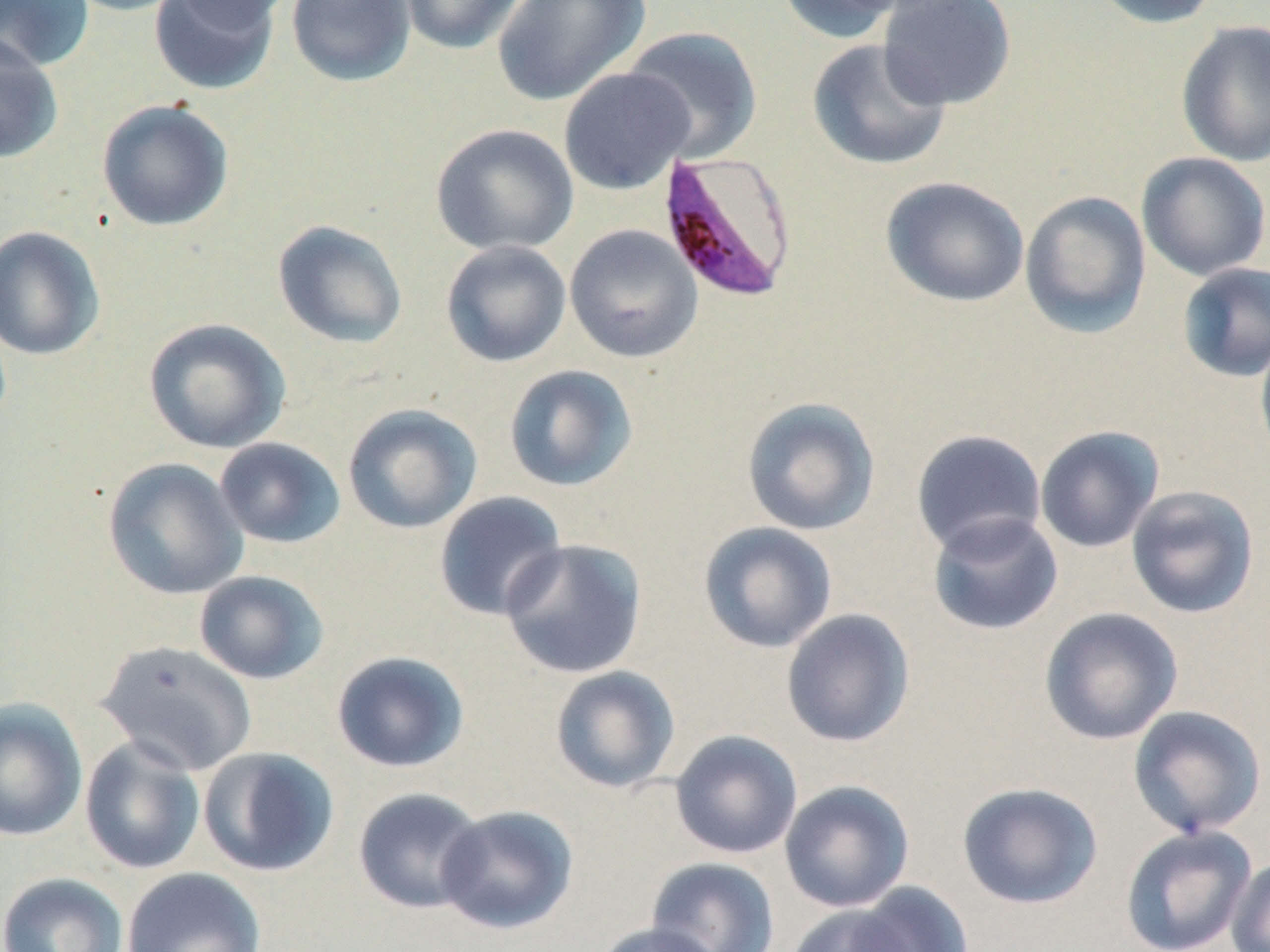 Approximate bounding boxes as (x1,y1)-(x2,y2) corner pairs in pixels. Uninfected red blood cell locations: (0,0)-(94,72), (57,0)-(190,17), (148,0)-(281,96), (164,0)-(293,31), (286,0)-(416,88), (398,0)-(528,55), (492,0)-(651,107), (774,0)-(914,44), (878,0)-(1017,110), (1085,0)-(1223,29), (1175,20)-(1270,168), (622,27)-(764,163), (0,31)-(63,164), (806,38)-(952,171), (558,67)-(695,195), (96,99)-(234,231), (430,123)-(579,256), (1136,152)-(1270,282), (881,176)-(1030,308), (1020,191)-(1151,338), (272,219)-(408,350), (564,223)-(703,363), (0,225)-(106,361), (440,240)-(572,367), (1177,262)-(1270,383), (143,317)-(291,454), (1255,333)-(1270,464), (503,364)-(638,492), (741,397)-(881,536), (342,403)-(483,534), (1034,425)-(1165,554), (910,429)-(1047,557), (214,437)-(346,549), (101,457)-(249,600), (1126,485)-(1260,619), (433,491)-(568,622), (927,512)-(1064,636), (698,521)-(838,654), (499,538)-(648,679), (193,570)-(328,684), (1038,606)-(1184,745), (780,608)-(916,747), (95,640)-(258,777), (330,650)-(470,774), (549,665)-(681,794), (0,698)-(88,841), (1127,705)-(1267,838), (669,730)-(803,859), (79,735)-(206,875), (197,746)-(340,877), (779,780)-(915,913), (956,781)-(1103,910), (352,787)-(487,915), (436,805)-(578,935), (1119,825)-(1257,952), (1226,856)-(1270,952), (645,857)-(781,952), (121,866)-(267,952), (0,872)-(128,952), (839,882)-(974,952), (785,904)-(918,952), (593,921)-(728,952). Plasmodium falciparum-infected red blood cell locations: (654,150)-(799,303). Slide-level diagnosis: Plasmodium falciparum. Captured at 1000x magnification. Thin blood smear. One field of a larger specimen. May-Grünwald-Giemsa-stained preparation. Image is 1270×952 pixels. Light microscopy.